Look for Plasmodium parasites.
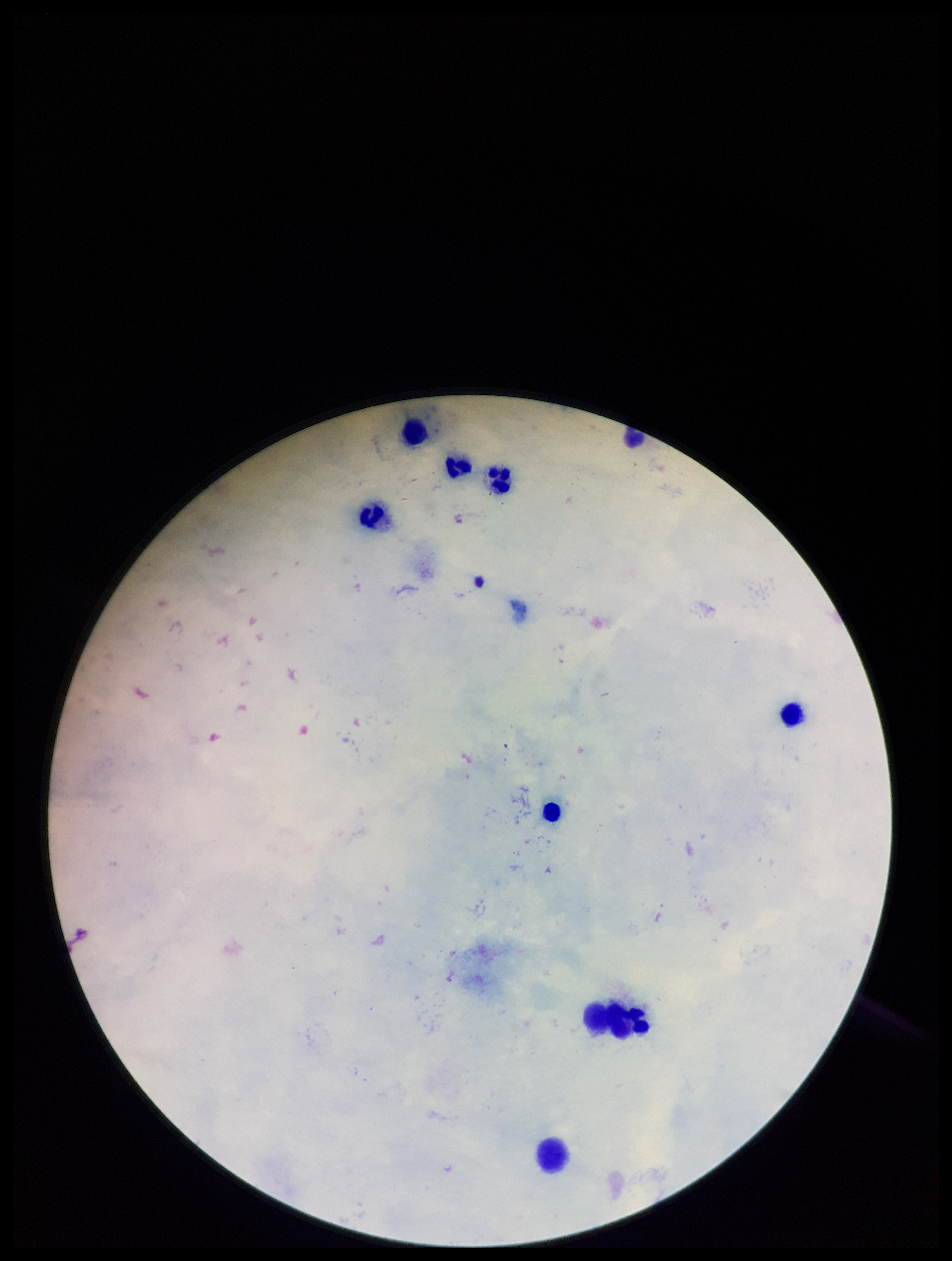
None detected.

{
  "leukocyte_count": 9,
  "image_size": "952×1261 pixels",
  "patient_malaria_status": "negative",
  "preparation": "thick blood smear",
  "capture": "smartphone photograph through the microscope eyepiece",
  "field_of_view": "single",
  "stain": "Giemsa",
  "parasite_count": 0
}